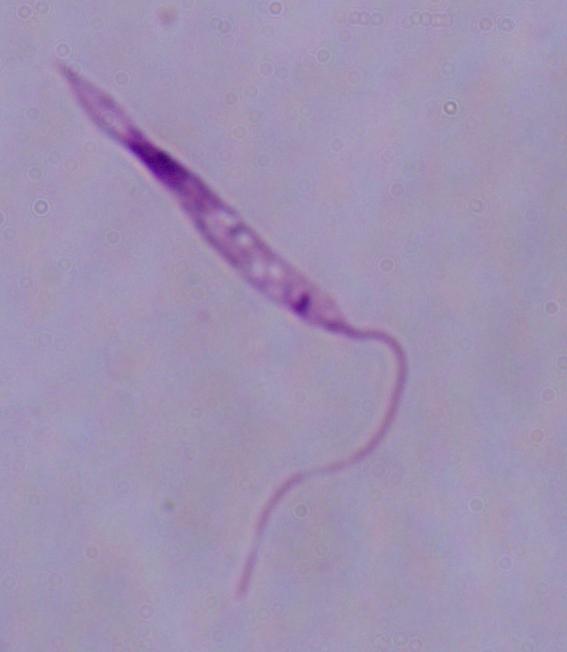
A Leishmania parasite is shown. Captured at 1000x magnification. Micrograph.